State which parasite is depicted.
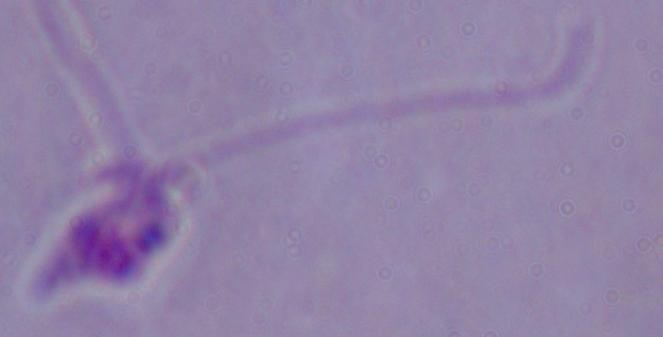

Leishmania.

Summary:
  - Modality: photomicrograph
  - Magnification: 1000x